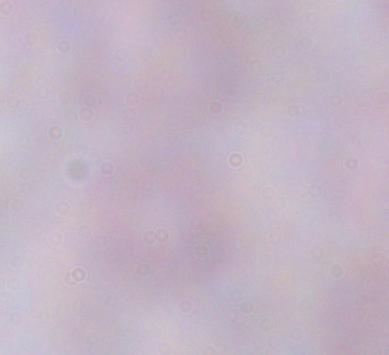 Micrograph. 1000x magnification. A trypanosome is seen.